Classify this cell by malaria status.
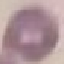
It is uninfected.

Acquired by smartphone through the microscope eyepiece. Thin blood film. Automatically extracted cell patch, resized to 64 × 64 pixels. Giemsa stain.